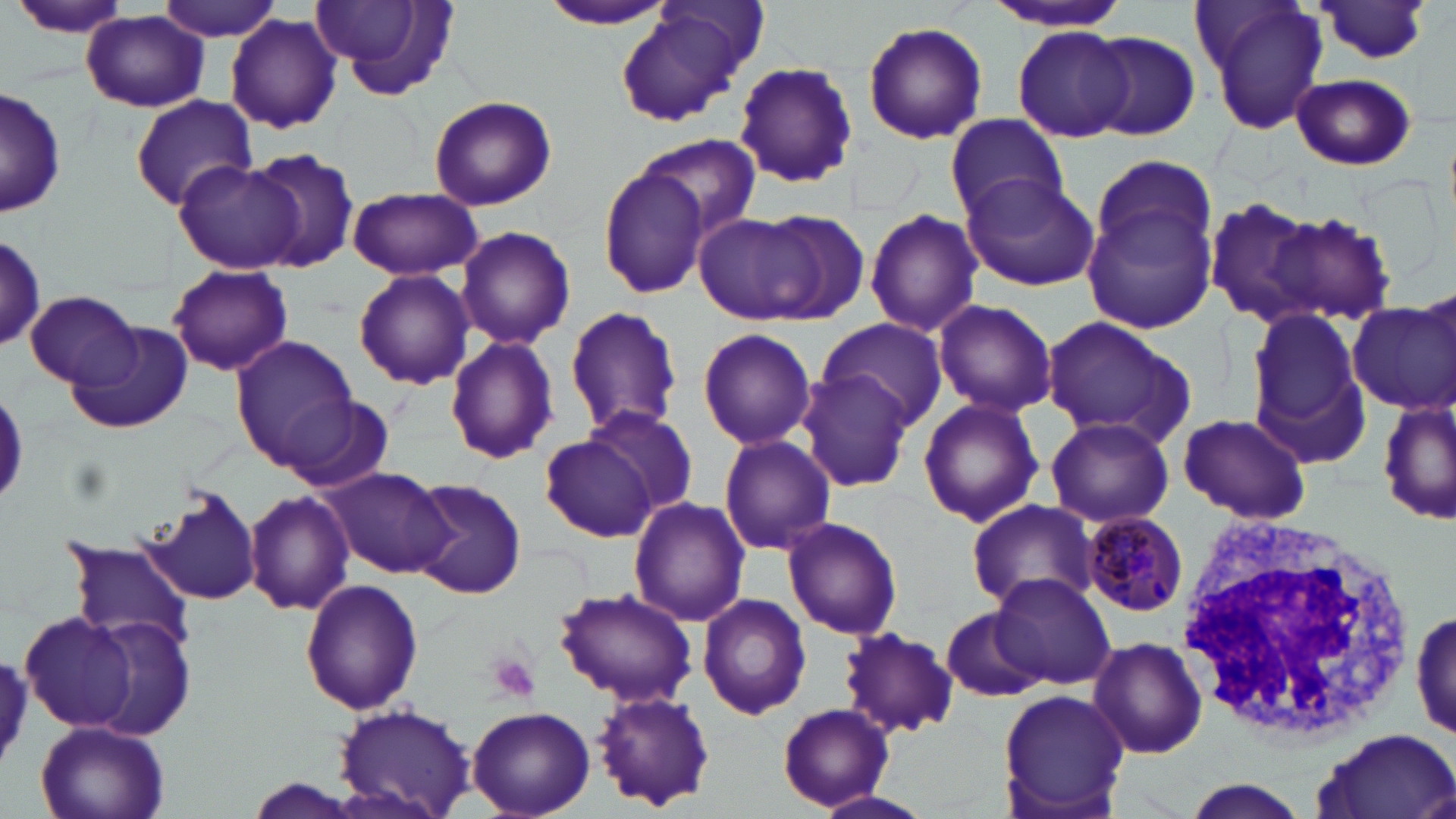 Approximate bounding boxes as (x1,y1)-(x2,y2) corner pairs in pixels. White blood cell locations: (1179,507)-(1422,747). Plasmodium malariae-infected red blood cell locations: (1079,511)-(1190,617). Uninfected red blood cell locations: (7,0)-(135,41), (155,0)-(285,42), (310,0)-(459,100), (1192,0)-(1331,137), (537,1)-(679,31), (981,2)-(1138,34), (1315,3)-(1435,68), (613,7)-(755,127), (81,10)-(210,113), (225,13)-(343,135), (862,21)-(987,143), (1013,26)-(1136,142), (1086,32)-(1200,140), (732,58)-(858,190), (1290,73)-(1417,170), (1,87)-(67,216), (129,96)-(258,210), (427,96)-(556,212), (941,114)-(1067,226), (638,133)-(761,239), (246,149)-(361,273), (1088,152)-(1219,278), (171,159)-(301,275), (596,165)-(710,298), (958,171)-(1100,291), (346,188)-(483,281), (1204,198)-(1329,327), (1084,201)-(1219,331), (747,208)-(870,322), (1260,208)-(1397,326), (865,209)-(983,336), (693,212)-(820,325), (456,226)-(576,351), (0,230)-(49,352), (166,265)-(294,376), (353,269)-(476,391), (1419,283)-(1455,390), (23,291)-(144,389), (1349,298)-(1456,415), (932,299)-(1058,420), (564,306)-(684,436), (1242,308)-(1370,452), (1039,315)-(1194,446), (815,318)-(948,430), (68,320)-(192,436), (697,327)-(816,450), (230,335)-(358,466), (444,336)-(559,464), (797,372)-(916,493), (1378,394)-(1454,527), (917,395)-(1045,528), (278,396)-(394,494), (582,406)-(701,519), (1176,412)-(1313,525), (1044,416)-(1174,528), (718,435)-(837,555), (541,436)-(655,541), (323,466)-(453,578), (409,478)-(526,599), (144,485)-(264,609), (244,489)-(354,614), (627,496)-(751,628), (964,497)-(1098,612), (782,517)-(903,641), (62,540)-(195,649), (991,573)-(1116,688), (300,577)-(424,715), (555,587)-(697,710), (697,593)-(811,721), (943,608)-(1045,704), (20,610)-(141,731), (1411,611)-(1455,742), (81,614)-(196,741), (838,627)-(957,738), (1086,636)-(1209,760), (997,688)-(1133,816), (590,689)-(718,811), (333,701)-(480,816), (778,704)-(893,810), (466,705)-(594,815), (31,718)-(171,819), (1314,726)-(1456,819), (1179,777)-(1317,819), (810,789)-(932,819). Platelet locations: (487,653)-(541,703). Slide-level diagnosis: Plasmodium malariae. Light microscopy. Single field of view. Thin blood film. 1000x magnification. May-Grünwald-Giemsa-stained preparation. Image is 1456×819 pixels.